Report the malaria status of this cell.
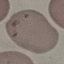

It is uninfected.

Summary:
  - Capture: smartphone camera at the microscope eyepiece
  - Image type: automatically extracted cell patch, resized to 64 × 64 pixels
  - Stain: Giemsa
  - Preparation: thin blood film